Outline each blood parasite and name the species.
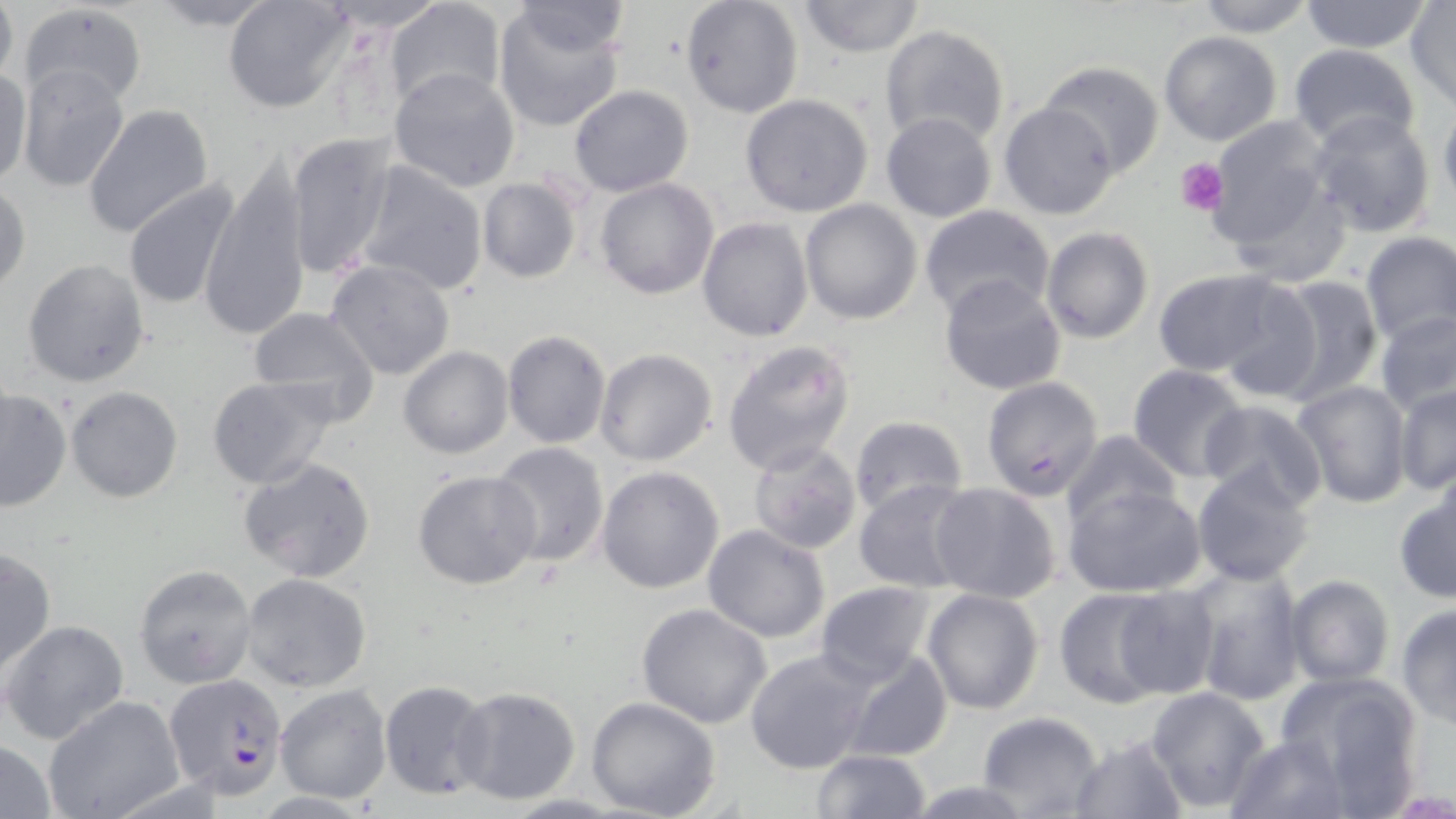
Approximate bounding boxes as [x1, y1, x2, y2] in pixels.
Plasmodium falciparum-infected red blood cells: [164, 672, 289, 799].
No Plasmodium ovale, Plasmodium malariae, Plasmodium vivax, Babesia divergens, or Trypanosoma brucei observed.

{
  "slide_level_diagnosis": "Plasmodium falciparum",
  "image_size": "1456×819 pixels",
  "stain": "May-Grünwald-Giemsa",
  "preparation": "thin blood smear",
  "platelet_locations": "approximate bounding boxes as [x1, y1, x2, y2] in pixels: [1178, 157, 1227, 216]",
  "magnification": "1000x",
  "field_of_view": "one of a larger specimen",
  "uninfected_red_blood_cell_locations": "approximate bounding boxes as [x1, y1, x2, y2] in pixels: [146, 0, 282, 31], [222, 0, 357, 114], [680, 0, 802, 117], [797, 0, 926, 57], [1193, 0, 1316, 37], [1299, 0, 1433, 54], [314, 1, 451, 33], [0, 2, 18, 91], [386, 2, 507, 113], [510, 3, 636, 58], [1406, 3, 1456, 108], [18, 4, 147, 111], [491, 5, 627, 133], [878, 24, 1011, 150], [1159, 31, 1283, 146], [1287, 44, 1421, 154], [1035, 61, 1167, 179], [17, 63, 132, 192], [388, 66, 521, 194], [0, 67, 31, 188], [568, 85, 694, 196], [739, 93, 874, 217], [998, 102, 1119, 221], [81, 103, 215, 239], [1439, 103, 1456, 211], [1306, 110, 1438, 240], [880, 112, 998, 224], [1203, 114, 1340, 264], [286, 132, 400, 279], [832, 152, 949, 286], [197, 158, 313, 342], [355, 159, 489, 296], [476, 176, 582, 282], [594, 178, 720, 300], [1, 180, 30, 298], [123, 181, 241, 311], [800, 199, 923, 324], [918, 203, 1054, 318], [697, 216, 814, 341], [1041, 228, 1152, 344], [1358, 230, 1455, 343], [322, 257, 457, 382], [23, 258, 150, 387], [1148, 269, 1293, 377], [1269, 273, 1384, 403], [938, 275, 1066, 395], [1208, 278, 1327, 402], [247, 307, 380, 424], [1376, 309, 1456, 415], [502, 330, 611, 447], [722, 339, 856, 475], [397, 346, 514, 459], [594, 347, 718, 467], [1127, 365, 1251, 483], [207, 374, 341, 489], [980, 376, 1104, 500], [1291, 379, 1412, 507], [1393, 384, 1456, 493], [0, 387, 71, 513], [65, 387, 183, 502], [1198, 401, 1328, 513], [848, 415, 968, 518], [1061, 429, 1182, 530], [749, 440, 861, 555], [490, 442, 610, 569], [238, 455, 377, 582], [1191, 464, 1317, 586], [596, 465, 724, 594], [412, 469, 541, 592], [853, 480, 974, 593], [929, 483, 1061, 603], [1064, 483, 1208, 597], [1394, 485, 1456, 602], [702, 524, 832, 643], [0, 548, 55, 677], [133, 564, 257, 688], [1186, 566, 1305, 703], [240, 573, 372, 692], [1284, 575, 1395, 688], [813, 581, 938, 685], [1108, 583, 1221, 702], [1053, 586, 1173, 709], [922, 588, 1045, 714], [635, 603, 772, 728], [1395, 604, 1456, 726], [2, 619, 130, 744], [745, 648, 875, 773], [842, 650, 954, 764], [1274, 671, 1426, 804], [377, 678, 495, 801], [275, 684, 392, 804], [1145, 685, 1272, 813], [454, 686, 582, 805], [43, 696, 184, 819], [585, 696, 721, 819], [974, 711, 1103, 818], [1066, 733, 1189, 817], [1224, 733, 1353, 817], [0, 739, 58, 817], [808, 750, 932, 819], [903, 780, 1037, 818]",
  "modality": "light microscopy"
}